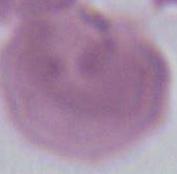

Summary:
  - Magnification: 1000x
  - Modality: micrograph
  - Identification: red blood cell